Classify this cell by malaria status.
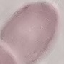

Uninfected.

Thin smear of blood. Automatically extracted cell patch, resized to 64 × 64 pixels. Photographed with a smartphone camera at the microscope eyepiece. Giemsa stain.